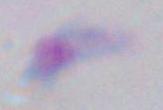
modality = micrograph
identification = Toxoplasma gondii
magnification = 1000x